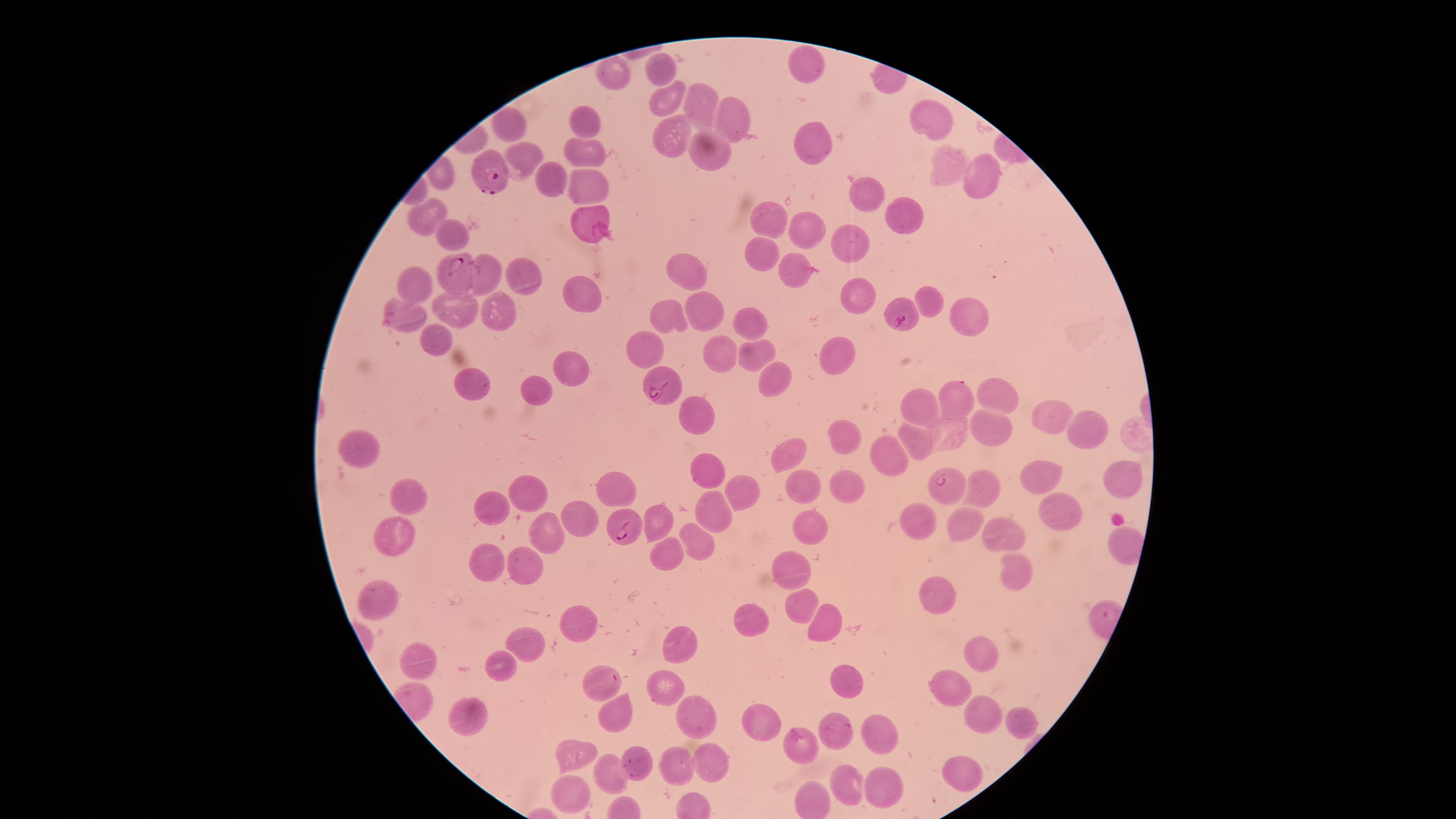

capture = smartphone photograph through the microscope eyepiece
stain = Giemsa
parasitized red blood cells = approximate marker points as (x, y) in pixels: (491, 166), (455, 272), (905, 320), (660, 386), (942, 480), (626, 527)
presence = malaria parasites identified
preparation = thin blood smear
uninfected red blood cells = approximate marker points as (x, y) in pixels: (808, 60), (617, 73), (663, 74), (669, 98), (701, 98), (927, 119), (732, 120), (584, 122), (515, 126), (814, 137), (667, 141), (590, 153), (702, 153), (526, 155), (948, 165), (978, 177), (549, 180), (591, 183), (866, 195), (908, 211), (429, 214), (773, 219), (589, 222), (805, 227), (448, 233), (850, 247), (764, 254), (685, 268), (798, 268), (522, 274), (489, 279), (419, 284), (581, 291), (854, 291), (929, 300), (464, 310), (706, 310), (493, 311), (965, 314), (404, 316), (669, 316), (749, 321), (432, 339), (648, 352), (848, 352), (754, 355), (722, 357), (568, 370), (771, 377), (473, 384), (535, 385), (998, 398), (953, 402), (925, 405), (697, 415), (1051, 419), (1086, 428), (985, 430), (840, 432), (946, 435), (917, 440), (364, 444), (789, 452), (882, 455), (708, 467), (1124, 475), (1037, 477), (616, 482), (806, 483), (848, 485), (526, 492), (983, 493), (737, 494), (406, 495), (492, 505), (1055, 507), (709, 511), (579, 514), (663, 519), (914, 521), (963, 524), (809, 529), (546, 532), (1010, 532), (396, 534), (701, 540), (664, 553), (496, 564), (530, 564), (1013, 565), (787, 567), (378, 598), (939, 598), (801, 606), (749, 618), (824, 621), (582, 627), (527, 643), (680, 644), (983, 656), (425, 659), (500, 663), (847, 679), (600, 684), (661, 691), (956, 694), (616, 710), (471, 715), (760, 719), (698, 720), (986, 720), (1018, 726), (832, 729), (879, 740), (805, 747), (582, 754), (637, 758), (708, 760), (677, 761), (962, 771), (615, 773), (853, 786), (878, 789), (574, 791)
field of view = single
image size = 1456×819 pixels
visible region = circular
species = Plasmodium falciparum